Classify this cell by malaria status.
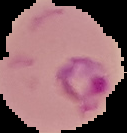
It is parasitized.

preparation = thin blood smear
image type = segmented cell region with the area outside set to black
image size = 127×133 pixels